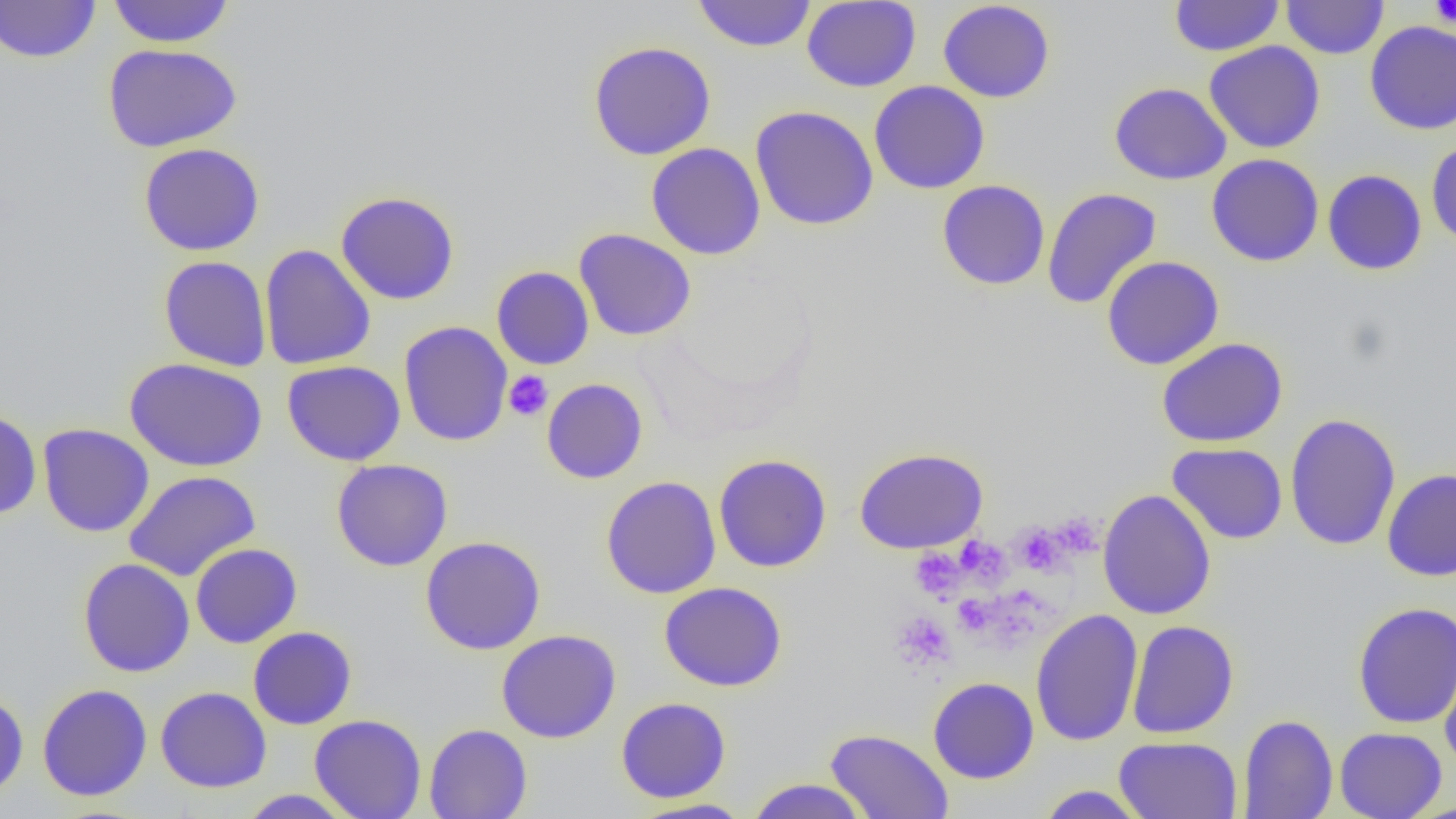
slide-level diagnosis = negative for blood parasites
image size = 1456×819 pixels
field of view = one of a larger specimen
uninfected red blood cell locations = approximate bounding boxes as (x1,y1)-(x2,y2) corner pairs in pixels: (0,0)-(101,64), (106,0)-(236,48), (691,0)-(816,52), (802,0)-(921,92), (1169,0)-(1284,56), (1281,0)-(1388,59), (937,1)-(1055,103), (1364,20)-(1456,135), (587,41)-(716,160), (1204,41)-(1326,153), (103,43)-(242,151), (868,80)-(990,194), (1109,82)-(1231,184), (750,105)-(879,231), (1426,139)-(1456,249), (138,142)-(266,256), (646,143)-(765,260), (1206,154)-(1324,267), (1322,169)-(1427,275), (937,180)-(1050,291), (1042,187)-(1162,310), (335,191)-(460,305), (573,228)-(697,341), (259,244)-(376,370), (1101,255)-(1224,370), (158,256)-(272,372), (491,266)-(595,370), (398,321)-(513,447), (1156,337)-(1288,448), (124,357)-(268,472), (282,360)-(406,466), (541,378)-(648,484), (0,409)-(43,520), (1284,412)-(1401,551), (38,424)-(154,537), (1167,442)-(1288,544), (854,447)-(989,553), (713,453)-(832,572), (331,459)-(453,571), (1382,467)-(1456,582), (123,470)-(261,582), (600,476)-(721,599), (1097,489)-(1216,620), (420,536)-(546,655), (190,543)-(302,648), (78,558)-(195,677), (659,581)-(788,691), (1352,601)-(1456,728), (1030,608)-(1143,747), (1127,620)-(1239,738), (248,626)-(357,729), (496,629)-(622,743), (1438,636)-(1456,776), (928,677)-(1039,784), (37,684)-(152,801), (155,686)-(272,792), (0,690)-(29,799), (616,696)-(731,803), (309,714)-(427,819), (1238,714)-(1337,819), (423,723)-(532,818), (1334,727)-(1447,819), (824,728)-(954,819), (1114,736)-(1242,819), (743,777)-(872,818), (1035,785)-(1149,818), (237,789)-(356,818), (630,797)-(755,818)
modality = optical microscopy
platelet locations = approximate bounding boxes as (x1,y1)-(x2,y2) corner pairs in pixels: (1430,0)-(1456,27), (503,370)-(553,421), (1053,512)-(1104,557), (1013,523)-(1064,574), (957,536)-(1011,587), (911,549)-(964,600), (954,595)-(992,634), (891,610)-(956,671)
magnification = 1000x
preparation = thin blood smear